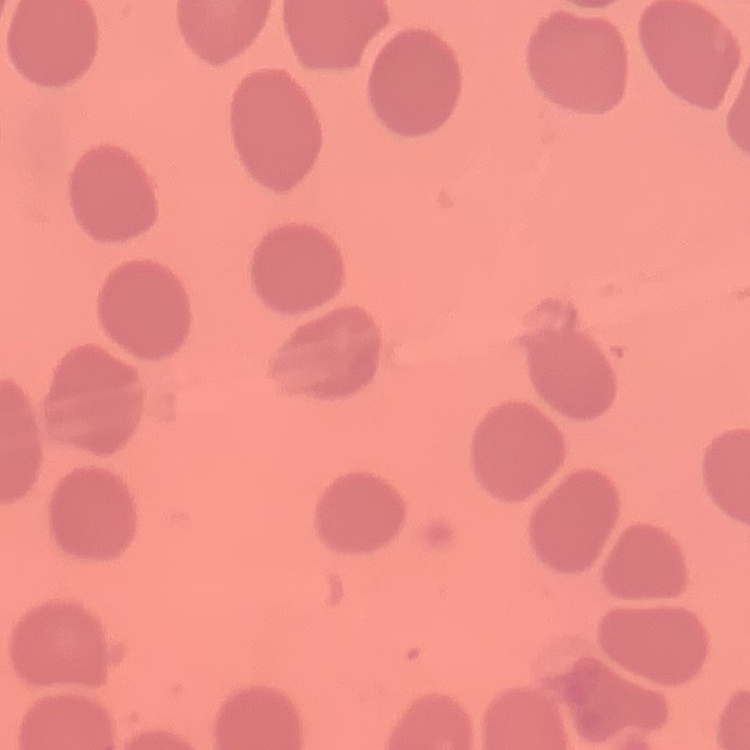
red blood cell morphology = no rouleaux formation
preparation = thin blood film
image type = square crop of a larger photomicrograph
stain = Field's or Giemsa